Outline each blood parasite and name the species.
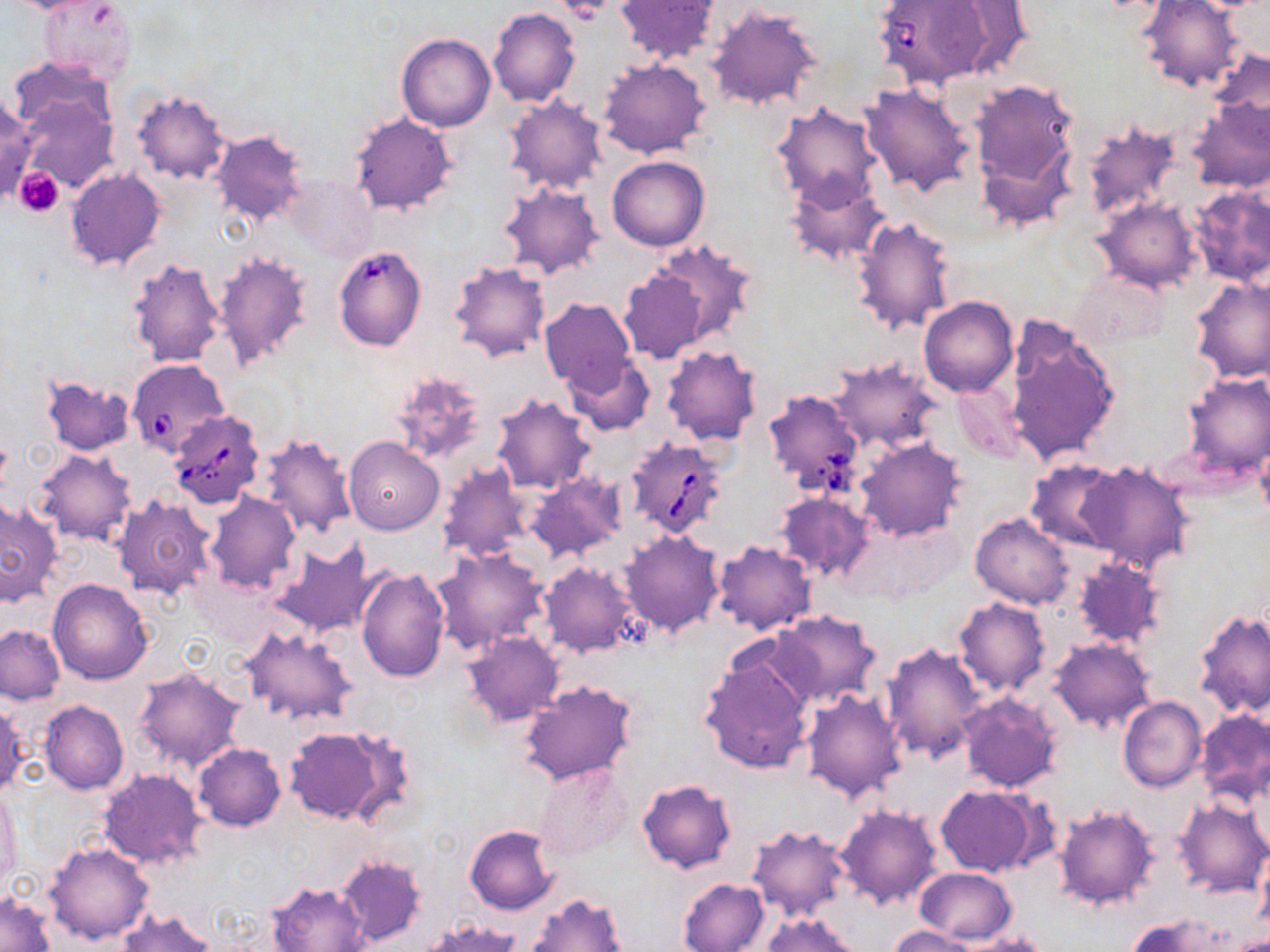

Approximate bounding boxes as (x1,y1)-(x2,y2) corner pairs in pixels.
Babesia divergens-infected red blood cells: (872,0)-(998,90), (333,244)-(428,351), (128,359)-(230,459), (763,389)-(866,496), (168,410)-(265,508), (624,436)-(729,539).
No Plasmodium falciparum, Plasmodium ovale, Plasmodium malariae, Plasmodium vivax, or Trypanosoma brucei observed.

Uninfected red blood cell locations: (614,0)-(723,66), (1136,1)-(1248,93), (935,2)-(1039,79), (707,5)-(824,112), (487,8)-(581,107), (396,33)-(495,131), (1201,47)-(1270,144), (597,58)-(711,159), (971,80)-(1079,199), (860,82)-(975,197), (14,90)-(118,195), (132,90)-(232,185), (0,91)-(37,205), (504,95)-(607,194), (1186,98)-(1269,192), (772,102)-(882,209), (349,114)-(458,216), (1081,120)-(1182,221), (209,130)-(308,225), (607,154)-(709,251), (66,169)-(166,270), (282,175)-(378,263), (785,175)-(891,266), (499,181)-(605,280), (1186,185)-(1270,286), (1093,197)-(1202,292), (850,215)-(955,336), (641,240)-(760,349), (212,250)-(312,372), (126,256)-(226,366), (448,260)-(552,363), (618,261)-(718,363), (1072,271)-(1169,348), (1190,275)-(1270,384), (539,297)-(638,397), (918,298)-(1017,396), (1005,320)-(1121,465), (661,346)-(762,446), (566,354)-(655,436), (828,358)-(942,453), (389,369)-(486,464), (1180,371)-(1270,478), (40,376)-(135,456), (949,382)-(1027,463), (491,393)-(597,495), (259,431)-(358,540), (343,436)-(444,534), (855,437)-(968,541), (32,449)-(138,545), (1025,459)-(1123,553), (1075,459)-(1195,573), (437,462)-(532,565), (527,473)-(628,566), (205,491)-(302,594), (774,491)-(875,582), (114,496)-(219,602), (0,499)-(62,606), (970,513)-(1074,609), (619,530)-(724,637), (712,540)-(816,635), (271,541)-(380,638), (433,548)-(549,656), (1072,557)-(1167,649), (540,561)-(642,657), (356,568)-(450,682), (48,578)-(154,684), (953,597)-(1051,696), (1193,609)-(1270,718), (771,610)-(881,708), (1,624)-(66,704), (242,626)-(356,727), (463,630)-(562,728), (1051,638)-(1156,733), (880,641)-(989,762), (697,652)-(815,776), (133,665)-(245,771), (518,680)-(640,786), (801,689)-(908,802), (959,691)-(1063,793), (1118,695)-(1206,791), (38,699)-(127,795), (0,700)-(28,798), (1197,711)-(1270,805), (283,725)-(402,825), (194,743)-(286,831), (534,762)-(632,861), (98,768)-(207,871), (636,779)-(737,873), (934,785)-(1037,877), (0,790)-(21,893), (1175,798)-(1269,898), (1054,803)-(1159,911), (836,804)-(942,911), (746,823)-(853,925), (465,825)-(558,914), (44,841)-(154,946), (1256,850)-(1270,931), (335,855)-(427,947), (915,866)-(1016,943), (678,877)-(769,952), (268,881)-(368,952), (1,892)-(55,952), (526,893)-(630,952), (116,909)-(214,952), (760,912)-(861,952), (1128,915)-(1228,952), (421,920)-(523,951), (889,925)-(979,952), (946,934)-(1053,952). Platelet locations: (557,1)-(614,23), (14,167)-(65,218). Slide-level diagnosis: Babesia divergens. Image is 1270×952 pixels. Thin blood film. May-Grünwald-Giemsa-stained preparation. Single field of view. 1000x magnification. Optical microscopy.